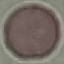
Malaria status: uninfected. Cell patch, automatically extracted from a larger field of view and resized to 64 × 64 pixels. Acquired by smartphone through the microscope eyepiece. Thin smear of blood. Giemsa-stained preparation.